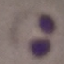

Summary:
  - Result: malaria parasites detected
  - Capture: smartphone camera at the microscope eyepiece
  - Image type: cell patch, automatically extracted from a larger field of view and resized to 64 × 64 pixels
  - Preparation: thin smear
  - Stain: Giemsa